Describe the morphology of the erythrocytes.
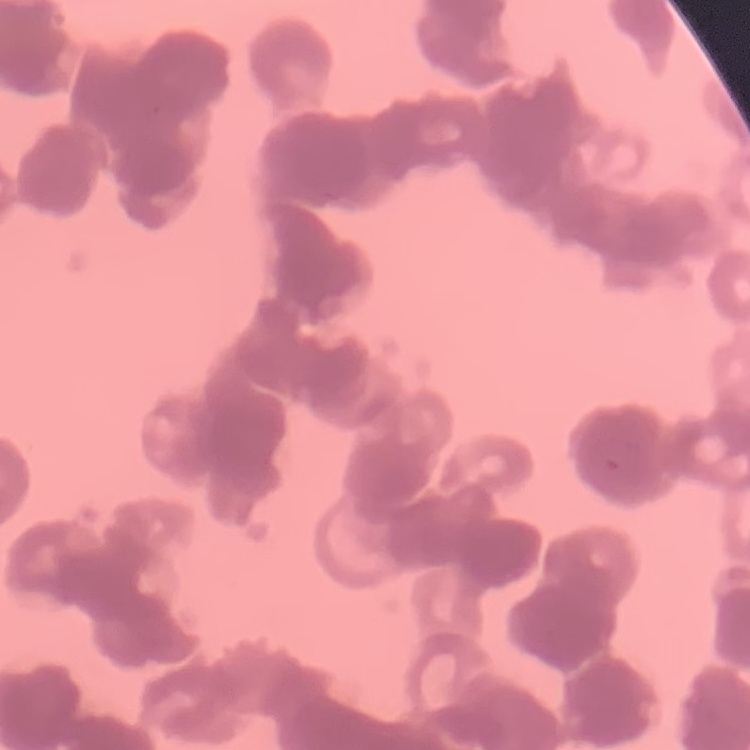

Rouleaux formation.

Summary:
  - Image type: one tile cut from a larger photomicrograph
  - Preparation: thin blood film
  - Stain: Field's or Giemsa